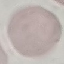

Result: no malaria parasites detected. Photographed with a smartphone camera at the microscope eyepiece. Giemsa stain. Cell patch, automatically extracted from a larger field of view and resized to 64 × 64 pixels. Thin smear of blood.